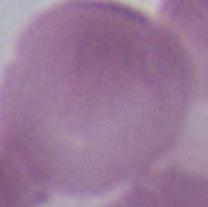

Summary:
  - Magnification: 1000x
  - Modality: micrograph
  - Identification: red blood cell